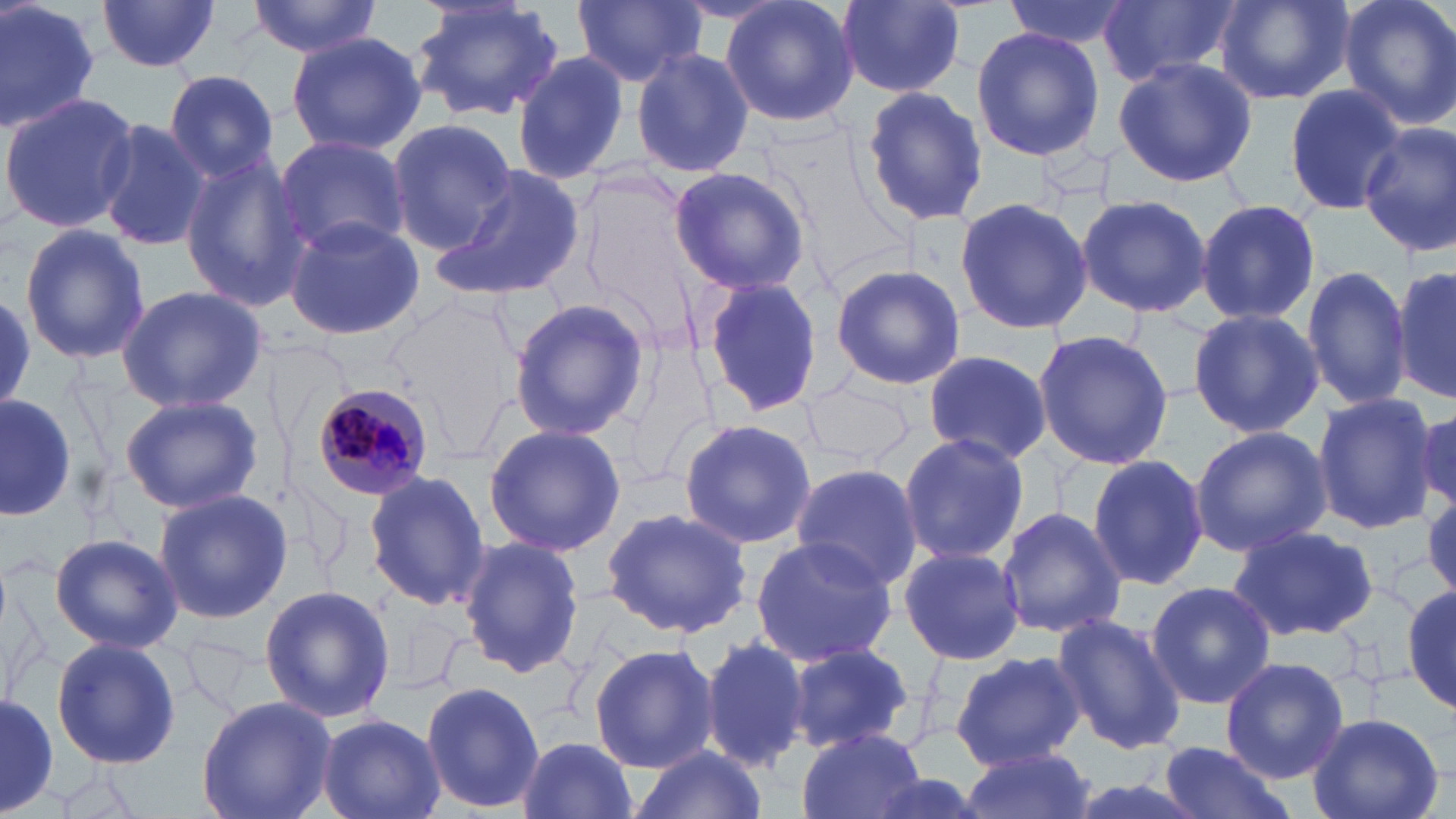
slide_level_diagnosis: Plasmodium malariae
stain: May-Grünwald-Giemsa
uninfected_red_blood_cell_locations: 'approximate bounding boxes as (x1, y1, x2, y2) in pixels: (0, 0, 102, 137), (247, 0, 381, 57), (406, 0, 565, 123), (574, 0, 704, 88), (721, 0, 858, 130), (834, 0, 969, 98), (1005, 0, 1134, 51), (1098, 0, 1244, 88), (1212, 0, 1354, 106), (1338, 0, 1456, 131), (95, 1, 223, 73), (971, 25, 1104, 162), (286, 31, 427, 157), (630, 44, 755, 181), (513, 51, 629, 183), (1113, 56, 1257, 189), (162, 69, 282, 183), (1282, 83, 1405, 213), (859, 85, 987, 227), (0, 90, 140, 235), (95, 117, 209, 252), (387, 118, 517, 252), (1358, 121, 1456, 257), (274, 135, 412, 256), (179, 151, 310, 312), (439, 162, 588, 301), (666, 165, 812, 295), (1075, 193, 1215, 320), (953, 196, 1093, 336), (1197, 199, 1320, 323), (283, 213, 425, 342), (18, 225, 151, 365), (829, 264, 966, 391), (1300, 264, 1411, 411), (1393, 264, 1454, 403), (698, 274, 827, 421), (115, 285, 266, 413), (505, 299, 650, 440), (1188, 308, 1323, 438), (1032, 330, 1174, 469), (613, 343, 724, 490), (920, 351, 1056, 467), (801, 377, 914, 472), (1309, 389, 1436, 536), (0, 394, 82, 524), (119, 394, 263, 513), (1412, 407, 1453, 511), (678, 417, 815, 549), (483, 423, 627, 554), (1190, 425, 1332, 557), (898, 430, 1029, 569), (1086, 454, 1210, 589), (788, 462, 922, 595), (361, 468, 489, 614), (150, 488, 294, 625), (996, 506, 1128, 640), (600, 507, 753, 640), (1226, 524, 1380, 643), (49, 532, 183, 653), (458, 535, 588, 678), (748, 535, 900, 668), (897, 545, 1025, 667), (0, 572, 55, 711), (1146, 580, 1278, 710), (259, 584, 396, 724), (1403, 584, 1456, 713), (1050, 612, 1186, 756), (700, 635, 813, 769), (50, 636, 181, 768), (587, 643, 720, 773), (784, 643, 915, 752), (951, 650, 1084, 769), (1220, 658, 1349, 784), (419, 680, 546, 814), (0, 687, 60, 818), (196, 696, 336, 819), (1307, 712, 1444, 819), (317, 713, 446, 819), (794, 728, 928, 819), (515, 734, 640, 819), (1157, 739, 1296, 819), (957, 744, 1098, 819), (631, 745, 768, 819)'
image_size: 1456×819 pixels
magnification: 1000x
field_of_view: one of a larger specimen
preparation: thin blood film
modality: light microscopy
plasmodium_malariae_infected_red_blood_cell_locations: 'approximate bounding boxes as (x1, y1, x2, y2) in pixels: (312, 383, 431, 501)'